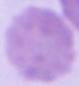

Micrograph. An erythrocyte is seen. Captured at 1000x magnification.